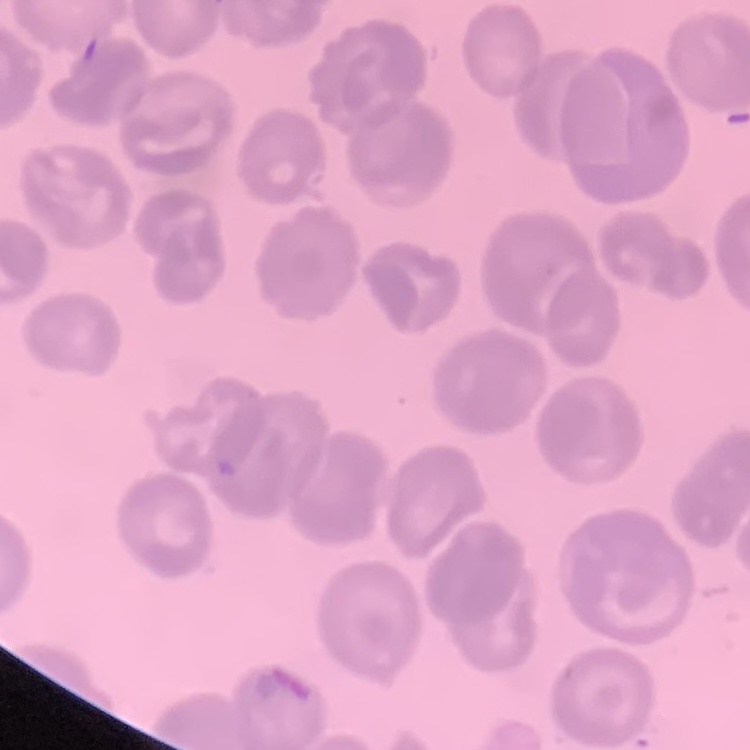

erythrocyte morphology = no rouleaux formation
stain = Field's or Giemsa
preparation = thin blood film
image type = square crop of a larger photomicrograph